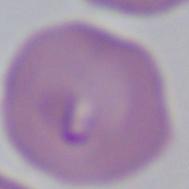

Summary:
  - Identification: Babesia
  - Modality: micrograph
  - Magnification: 1000x